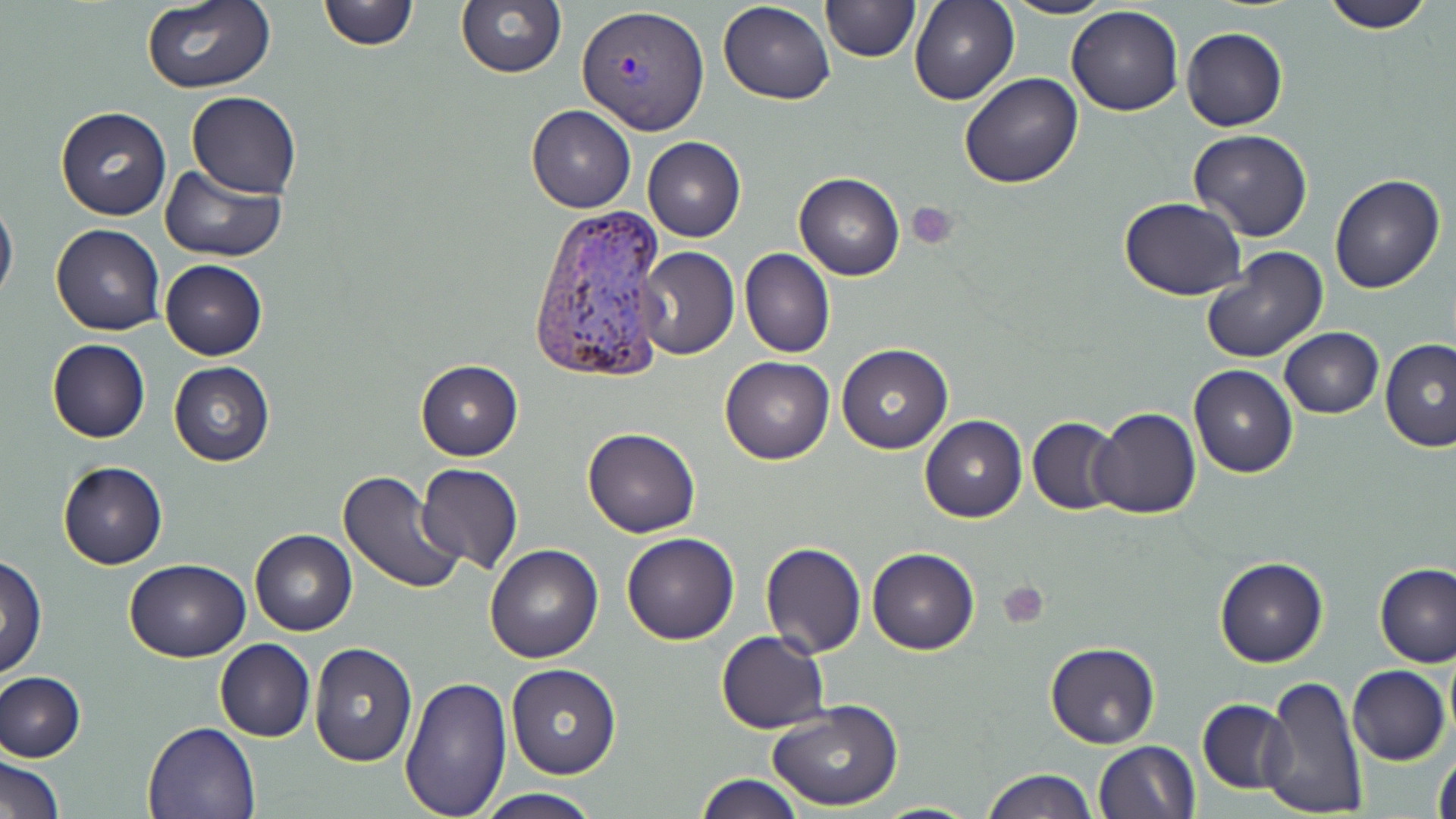

slide-level diagnosis = Plasmodium vivax
magnification = 1000x
uninfected red blood cell locations = approximate bounding boxes as named x1/y1/x2/y2 corners in pixels: (x1=456, y1=0, x2=566, y2=80), (x1=717, y1=0, x2=835, y2=104), (x1=822, y1=0, x2=918, y2=62), (x1=909, y1=0, x2=1018, y2=105), (x1=1004, y1=0, x2=1116, y2=20), (x1=1320, y1=0, x2=1438, y2=32), (x1=318, y1=1, x2=417, y2=50), (x1=139, y1=2, x2=276, y2=92), (x1=1065, y1=5, x2=1184, y2=116), (x1=1182, y1=27, x2=1287, y2=130), (x1=960, y1=73, x2=1082, y2=189), (x1=187, y1=92, x2=300, y2=200), (x1=526, y1=105, x2=635, y2=212), (x1=55, y1=106, x2=172, y2=221), (x1=1189, y1=129, x2=1313, y2=241), (x1=643, y1=136, x2=746, y2=241), (x1=161, y1=163, x2=288, y2=262), (x1=794, y1=172, x2=904, y2=280), (x1=1329, y1=172, x2=1446, y2=293), (x1=0, y1=193, x2=18, y2=306), (x1=1120, y1=197, x2=1248, y2=302), (x1=50, y1=223, x2=164, y2=335), (x1=636, y1=247, x2=740, y2=360), (x1=1201, y1=247, x2=1328, y2=363), (x1=740, y1=249, x2=834, y2=358), (x1=160, y1=259, x2=267, y2=360), (x1=1279, y1=327, x2=1384, y2=419), (x1=46, y1=338, x2=150, y2=442), (x1=1379, y1=338, x2=1456, y2=451), (x1=837, y1=344, x2=952, y2=454), (x1=720, y1=356, x2=833, y2=464), (x1=415, y1=360, x2=523, y2=460), (x1=168, y1=361, x2=274, y2=467), (x1=1188, y1=364, x2=1297, y2=478), (x1=1089, y1=407, x2=1201, y2=521), (x1=920, y1=416, x2=1027, y2=522), (x1=1027, y1=416, x2=1123, y2=515), (x1=583, y1=428, x2=700, y2=537), (x1=58, y1=461, x2=168, y2=569), (x1=416, y1=464, x2=523, y2=576), (x1=338, y1=470, x2=466, y2=597), (x1=250, y1=529, x2=356, y2=636), (x1=621, y1=532, x2=739, y2=645), (x1=759, y1=541, x2=867, y2=658), (x1=484, y1=545, x2=602, y2=663), (x1=868, y1=547, x2=978, y2=655), (x1=1, y1=556, x2=47, y2=680), (x1=124, y1=558, x2=251, y2=662), (x1=1214, y1=558, x2=1327, y2=667), (x1=1375, y1=563, x2=1455, y2=669), (x1=716, y1=631, x2=829, y2=733), (x1=214, y1=640, x2=315, y2=742), (x1=309, y1=640, x2=417, y2=766), (x1=1044, y1=642, x2=1161, y2=749), (x1=1444, y1=646, x2=1456, y2=746), (x1=507, y1=663, x2=620, y2=779), (x1=1347, y1=665, x2=1450, y2=765), (x1=1, y1=671, x2=86, y2=761), (x1=400, y1=675, x2=512, y2=819), (x1=1259, y1=675, x2=1367, y2=818), (x1=1197, y1=698, x2=1292, y2=793), (x1=767, y1=701, x2=903, y2=812), (x1=142, y1=722, x2=262, y2=817), (x1=1094, y1=740, x2=1199, y2=819), (x1=1432, y1=742, x2=1456, y2=819), (x1=2, y1=754, x2=65, y2=818), (x1=981, y1=768, x2=1096, y2=818), (x1=694, y1=775, x2=806, y2=818), (x1=478, y1=789, x2=604, y2=819), (x1=871, y1=799, x2=984, y2=817)
platelet locations = approximate bounding boxes as named x1/y1/x2/y2 corners in pixels: (x1=908, y1=202, x2=959, y2=249), (x1=999, y1=581, x2=1049, y2=628)
stain = May-Grünwald-Giemsa
modality = light microscopy
Plasmodium vivax-infected red blood cell locations = approximate bounding boxes as named x1/y1/x2/y2 corners in pixels: (x1=576, y1=7, x2=709, y2=132), (x1=527, y1=203, x2=668, y2=383)
image size = 1456×819 pixels
field of view = one of a larger specimen
preparation = thin blood film